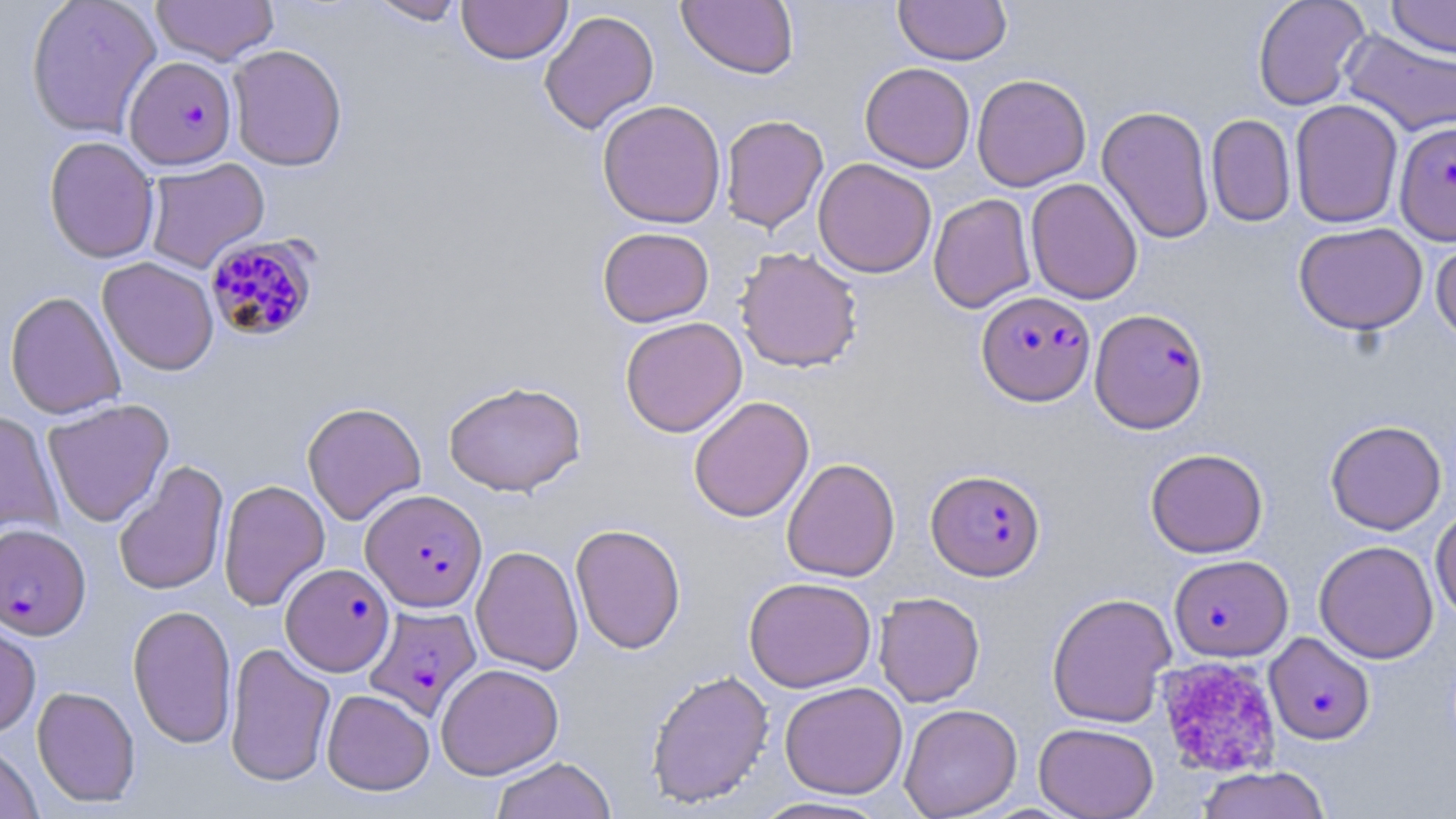

slide-level diagnosis = Plasmodium falciparum
stain = May-Grünwald-Giemsa
Plasmodium falciparum-infected red blood cell locations = approximate bounding boxes as (x1, y1, x2, y2) in pixels: (123, 55, 236, 170), (1395, 121, 1456, 244), (205, 234, 320, 342), (976, 290, 1096, 405), (1090, 308, 1208, 433), (926, 468, 1045, 581), (361, 489, 487, 612), (0, 522, 91, 640), (1169, 554, 1293, 661), (281, 562, 394, 676), (364, 603, 481, 720), (1264, 632, 1375, 745)
preparation = thin blood smear
uninfected red blood cell locations = approximate bounding boxes as (x1, y1, x2, y2) in pixels: (25, 0, 162, 139), (151, 0, 280, 65), (367, 0, 468, 25), (457, 0, 573, 65), (677, 0, 799, 79), (893, 0, 1012, 65), (1252, 0, 1370, 111), (1386, 0, 1456, 59), (539, 9, 659, 134), (1340, 29, 1456, 138), (227, 44, 347, 171), (860, 62, 975, 173), (972, 74, 1091, 191), (597, 99, 727, 229), (1290, 99, 1404, 228), (1097, 105, 1215, 245), (720, 114, 829, 233), (1206, 114, 1296, 227), (43, 136, 160, 264), (144, 157, 270, 273), (813, 158, 937, 278), (1025, 178, 1143, 305), (928, 193, 1037, 313), (1293, 222, 1428, 335), (597, 226, 714, 327), (1431, 235, 1456, 343), (734, 246, 863, 373), (97, 258, 219, 375), (5, 290, 126, 419), (620, 316, 748, 437), (443, 380, 585, 496), (688, 395, 815, 523), (42, 398, 174, 527), (301, 402, 426, 525), (0, 410, 64, 538), (1325, 419, 1447, 535), (1145, 448, 1268, 558), (782, 457, 900, 582), (113, 461, 229, 596), (218, 478, 330, 611), (1430, 506, 1456, 620), (570, 523, 686, 654), (1314, 540, 1439, 664), (471, 545, 584, 675), (743, 576, 877, 693), (874, 592, 985, 707), (1047, 592, 1177, 728), (127, 604, 237, 749), (0, 612, 41, 738), (225, 641, 336, 786), (435, 663, 564, 779), (645, 668, 775, 808), (779, 681, 908, 799), (32, 685, 141, 807), (321, 689, 435, 795), (899, 703, 1022, 818), (1034, 722, 1159, 819), (0, 739, 43, 819), (490, 756, 616, 819), (1196, 765, 1331, 819), (749, 796, 893, 818)
modality = optical microscopy
platelet locations = approximate bounding boxes as (x1, y1, x2, y2) in pixels: (1155, 656, 1283, 777)
image size = 1456×819 pixels
field of view = single
magnification = 1000x